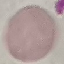
Malaria status: uninfected. Thin blood smear. Automatically extracted cell patch, resized to 64 × 64 pixels. Giemsa stain. Photographed with a smartphone camera at the microscope eyepiece.